Evaluate for malaria.
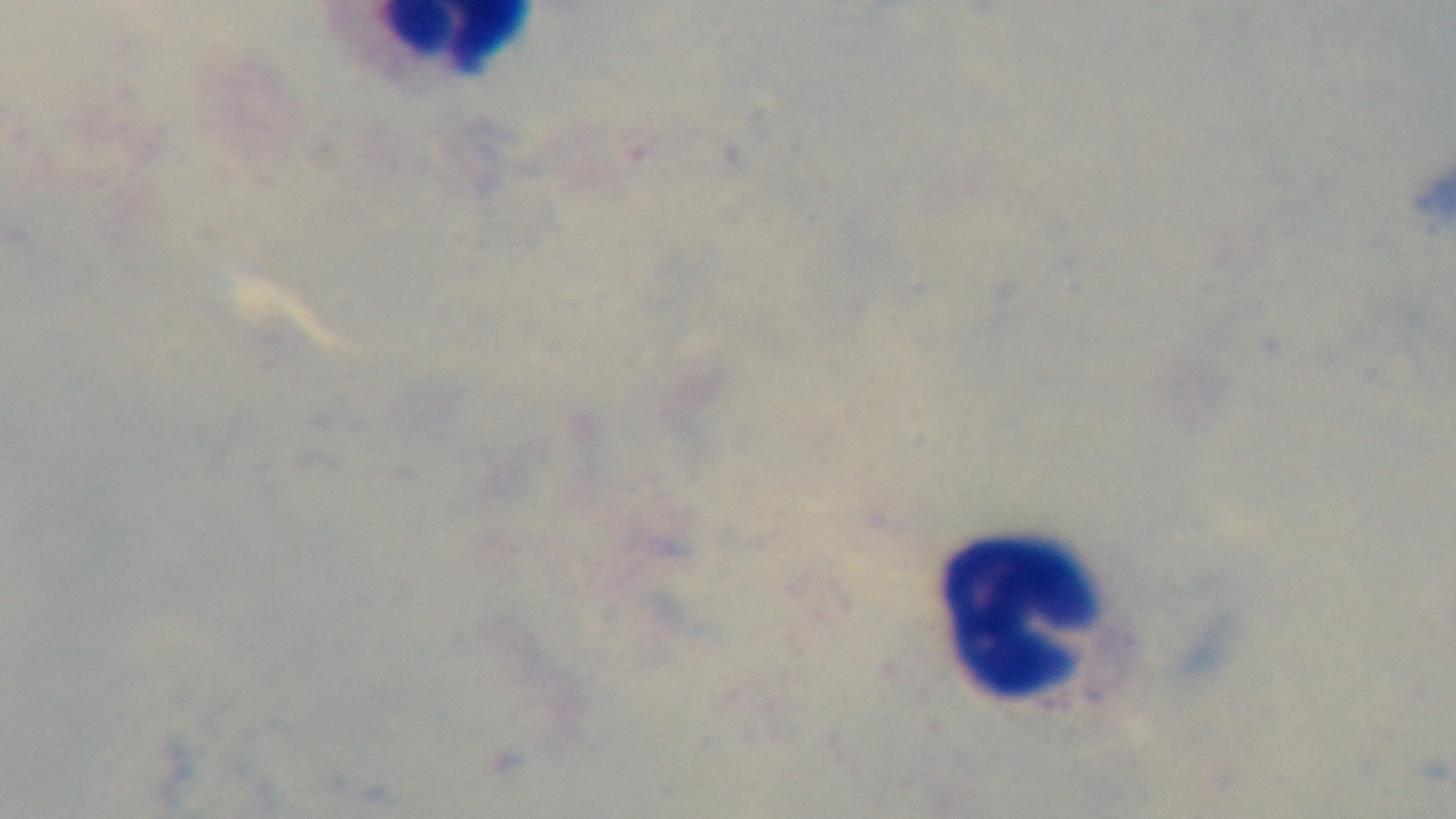

Negative.

preparation = thick
objective = 100x oil immersion
capture = mounted 4K digital camera
modality = light microscopy
field of view = single
stain = Giemsa